Describe the morphology of the red blood cells.
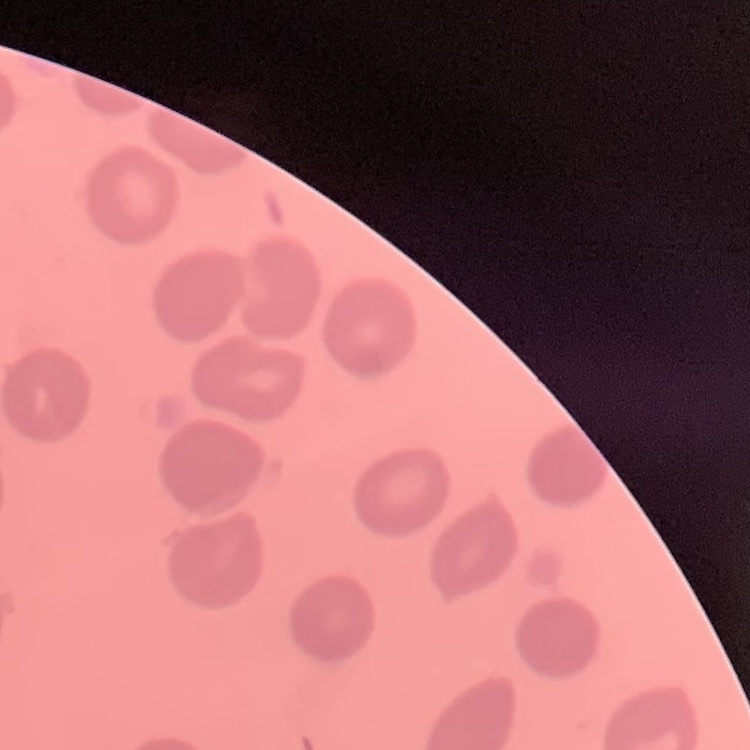

No rouleaux formation.

Summary:
  - Preparation: thin blood smear
  - Stain: Field's or Giemsa
  - Image type: one tile cut from a larger photomicrograph